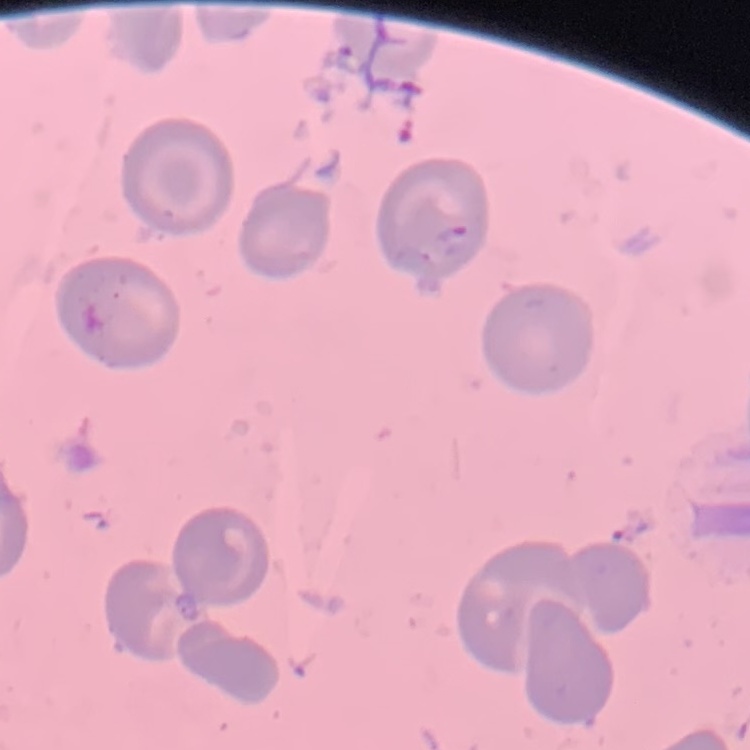

The erythrocytes show no rouleaux formation. Thin blood film. Square crop of a larger photomicrograph. Stained with either Field's or Giemsa.